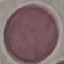
Summary:
  - Malaria status: uninfected
  - Capture: smartphone camera at the microscope eyepiece
  - Stain: Giemsa
  - Image type: automatically extracted cell patch, resized to 64 × 64 pixels
  - Preparation: thin blood film